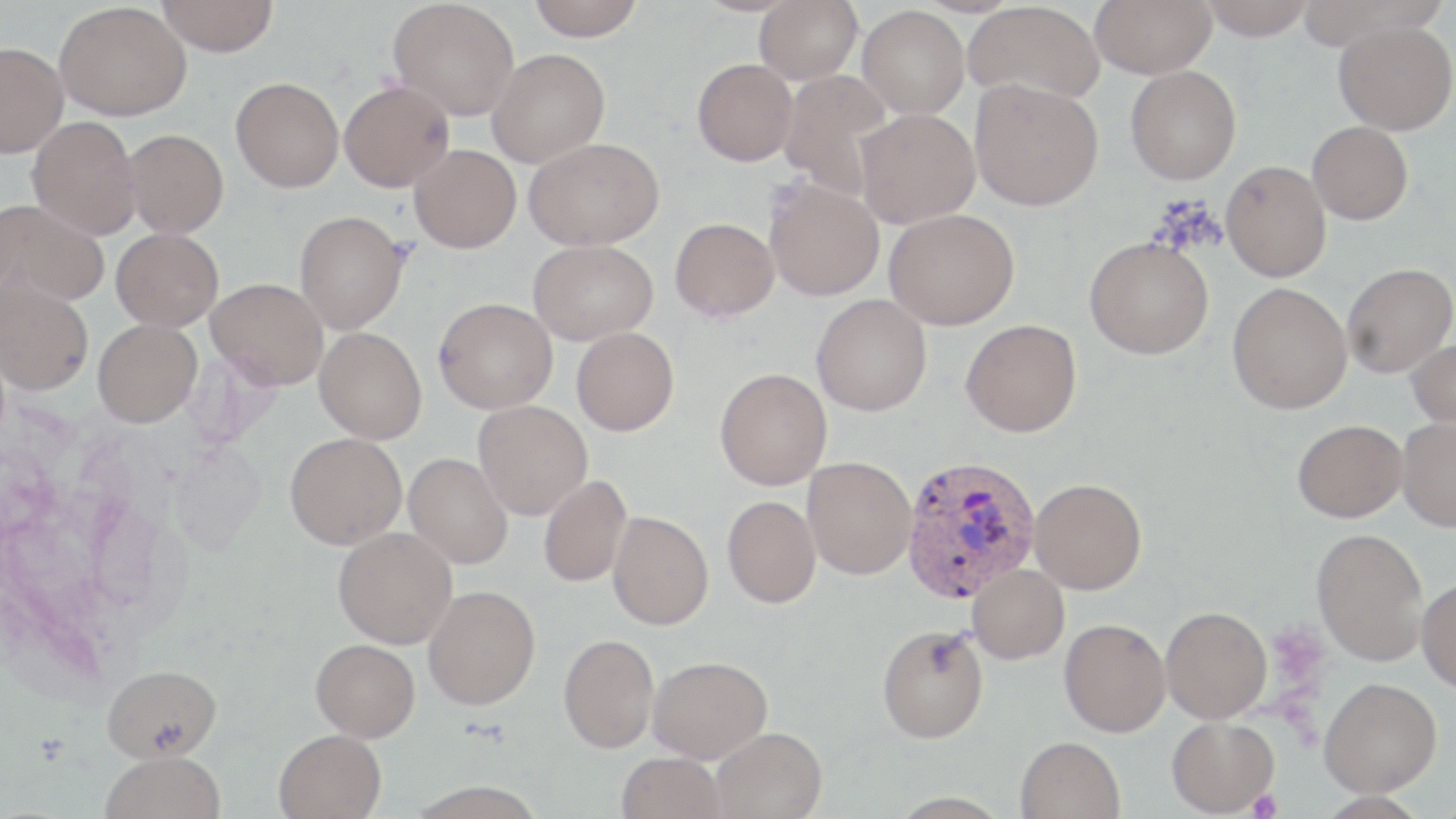 Approximate bounding boxes as named x1/y1/x2/y2 corners in pixels. Platelet locations: (x1=1246, y1=789, x2=1282, y2=818). Plasmodium vivax-infected red blood cell locations: (x1=900, y1=454, x2=1041, y2=603). Uninfected red blood cell locations: (x1=157, y1=0, x2=278, y2=56), (x1=388, y1=0, x2=520, y2=121), (x1=526, y1=0, x2=644, y2=40), (x1=754, y1=0, x2=862, y2=84), (x1=1090, y1=0, x2=1216, y2=78), (x1=1198, y1=0, x2=1316, y2=40), (x1=964, y1=1, x2=1105, y2=106), (x1=54, y1=2, x2=191, y2=121), (x1=857, y1=5, x2=970, y2=119), (x1=1334, y1=20, x2=1456, y2=135), (x1=0, y1=42, x2=68, y2=158), (x1=486, y1=48, x2=610, y2=168), (x1=692, y1=58, x2=797, y2=166), (x1=1125, y1=65, x2=1241, y2=185), (x1=778, y1=70, x2=896, y2=200), (x1=230, y1=76, x2=344, y2=192), (x1=970, y1=78, x2=1103, y2=211), (x1=339, y1=80, x2=454, y2=191), (x1=854, y1=108, x2=980, y2=228), (x1=27, y1=116, x2=141, y2=239), (x1=1307, y1=121, x2=1413, y2=224), (x1=123, y1=129, x2=228, y2=238), (x1=524, y1=137, x2=664, y2=250), (x1=409, y1=145, x2=521, y2=253), (x1=1221, y1=160, x2=1331, y2=282), (x1=764, y1=177, x2=884, y2=301), (x1=0, y1=198, x2=110, y2=307), (x1=883, y1=209, x2=1019, y2=330), (x1=294, y1=210, x2=408, y2=333), (x1=669, y1=218, x2=779, y2=322), (x1=111, y1=228, x2=224, y2=331), (x1=1084, y1=237, x2=1214, y2=359), (x1=528, y1=239, x2=657, y2=345), (x1=1342, y1=262, x2=1455, y2=378), (x1=0, y1=276, x2=94, y2=395), (x1=206, y1=278, x2=328, y2=389), (x1=1227, y1=282, x2=1352, y2=414), (x1=811, y1=294, x2=931, y2=416), (x1=434, y1=297, x2=558, y2=414), (x1=93, y1=319, x2=202, y2=427), (x1=960, y1=319, x2=1082, y2=437), (x1=314, y1=327, x2=427, y2=444), (x1=571, y1=327, x2=679, y2=436), (x1=1407, y1=338, x2=1456, y2=431), (x1=714, y1=368, x2=832, y2=490), (x1=473, y1=400, x2=592, y2=519), (x1=1397, y1=417, x2=1456, y2=531), (x1=1292, y1=419, x2=1407, y2=522), (x1=284, y1=432, x2=407, y2=549), (x1=404, y1=453, x2=513, y2=569), (x1=802, y1=457, x2=916, y2=579), (x1=538, y1=475, x2=632, y2=587), (x1=1029, y1=478, x2=1146, y2=594), (x1=722, y1=496, x2=821, y2=608), (x1=608, y1=511, x2=714, y2=630), (x1=333, y1=526, x2=457, y2=649), (x1=1311, y1=528, x2=1429, y2=665), (x1=967, y1=563, x2=1069, y2=663), (x1=1416, y1=576, x2=1456, y2=694), (x1=423, y1=585, x2=540, y2=710), (x1=1161, y1=606, x2=1272, y2=723), (x1=1059, y1=618, x2=1171, y2=737), (x1=877, y1=624, x2=989, y2=743), (x1=558, y1=634, x2=659, y2=753), (x1=311, y1=639, x2=420, y2=741), (x1=648, y1=655, x2=772, y2=763), (x1=102, y1=664, x2=221, y2=761), (x1=1318, y1=677, x2=1441, y2=797), (x1=1166, y1=716, x2=1279, y2=817), (x1=712, y1=727, x2=827, y2=819), (x1=274, y1=728, x2=386, y2=819), (x1=1015, y1=736, x2=1125, y2=819), (x1=101, y1=752, x2=226, y2=819), (x1=617, y1=752, x2=725, y2=819). Slide-level diagnosis: Plasmodium vivax. Optical microscopy. Thin blood smear. May-Grünwald-Giemsa-stained preparation. Image is 1456×819 pixels. Single field of view. Captured at 1000x magnification.